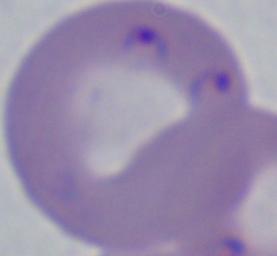 1000x magnification. A Babesia parasite is seen. Photomicrograph.